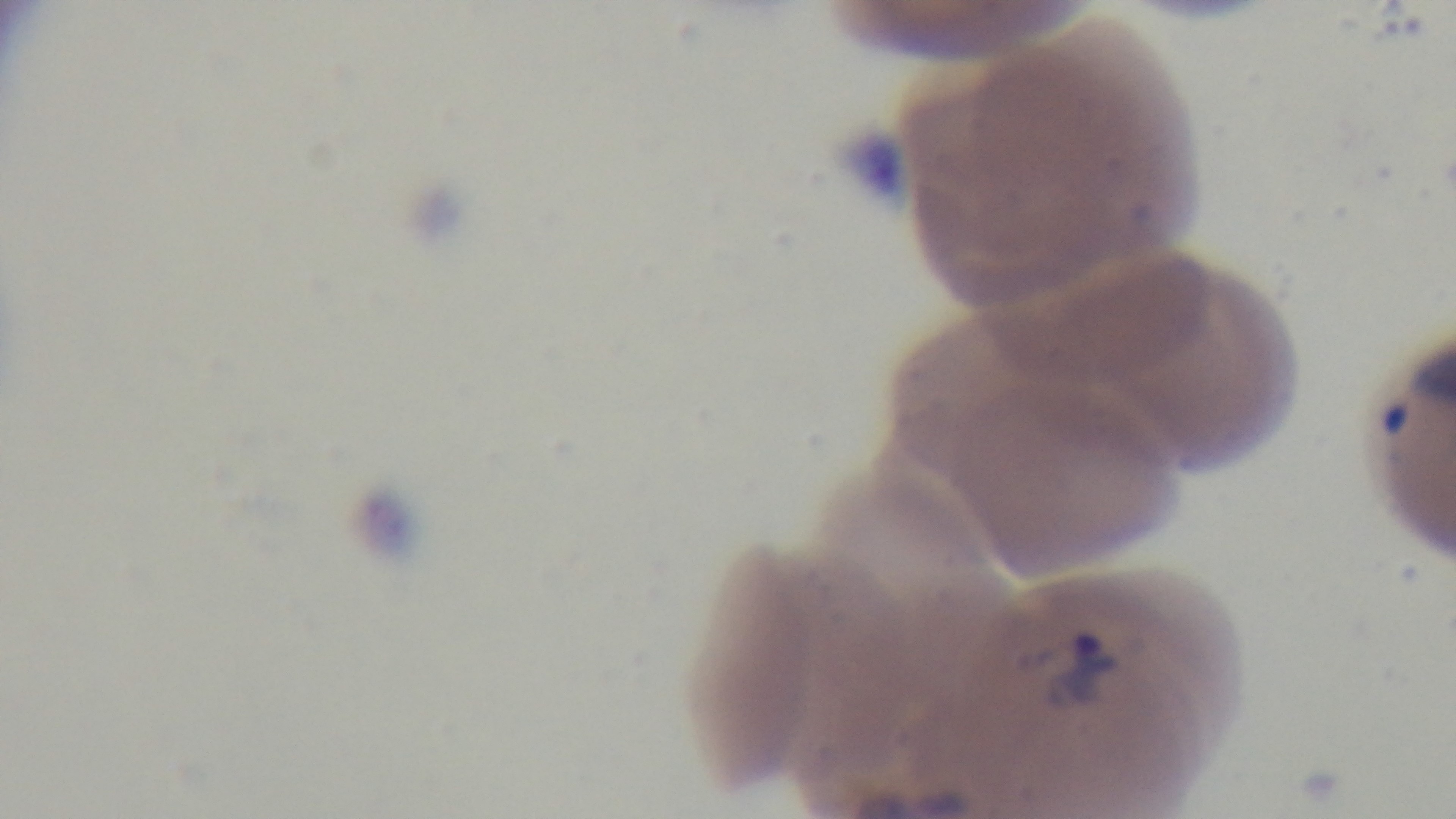
capture = mounted 4K digital camera
preparation = thin smear
field of view = single
malaria status = positive
modality = light microscopy
stain = Giemsa
objective = 100x oil immersion